Assess the morphology of the erythrocytes.
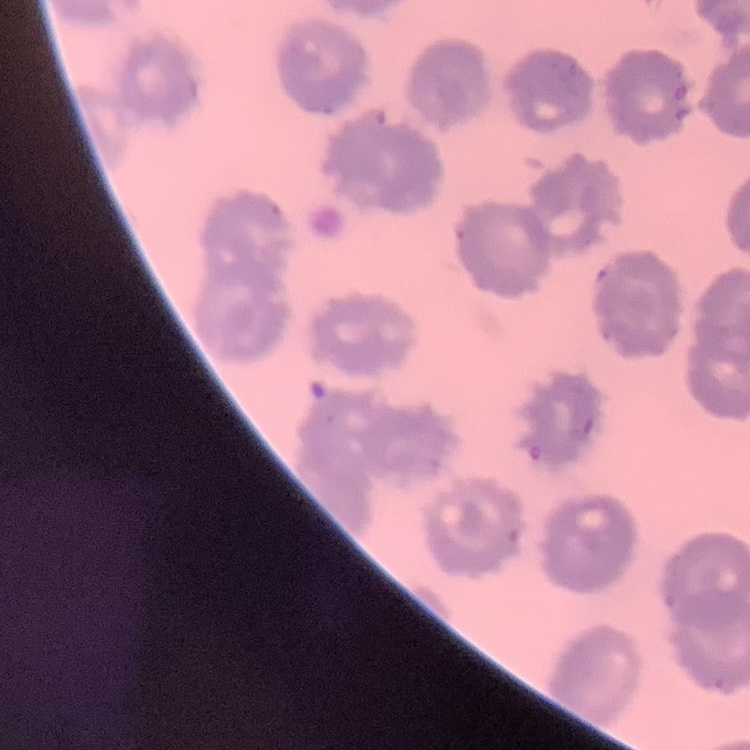

No rouleaux formation.

Thin blood smear. Field's or Giemsa stain. Square crop of a larger photomicrograph.